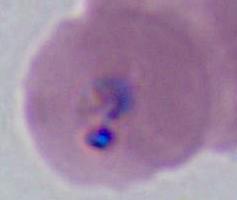
{
  "modality": "photomicrograph",
  "identification": "Plasmodium",
  "magnification": "400x or 1000x"
}